Locate every blood parasite and identify its species.
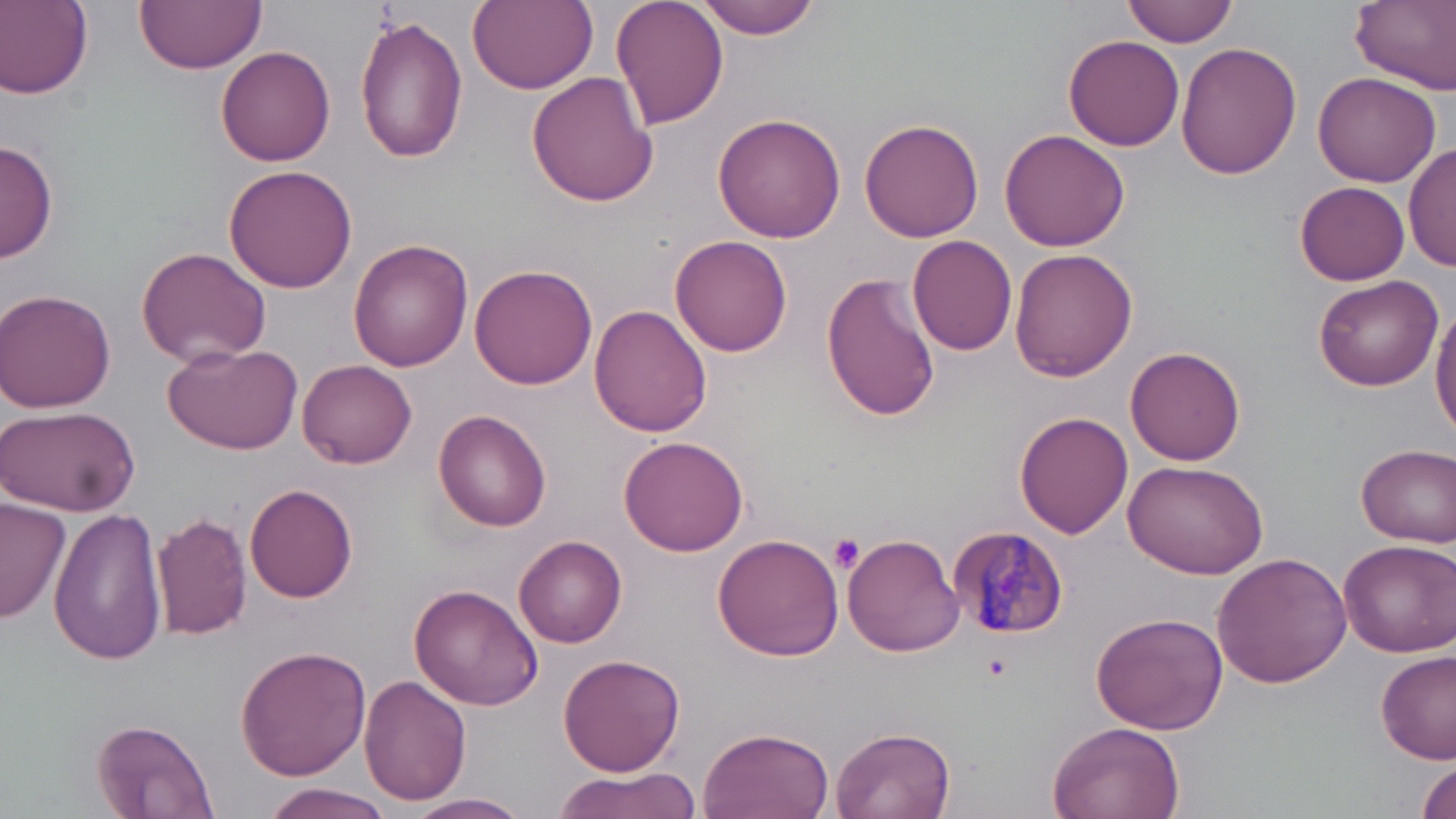

Approximate bounding boxes as (x1, y1, x2, y2) in pixels.
Plasmodium malariae-infected red blood cells: (948, 527, 1069, 640).
No Plasmodium falciparum, Plasmodium ovale, Plasmodium vivax, Babesia divergens, or Trypanosoma brucei observed.

Platelet locations: (829, 534, 865, 571). Uninfected red blood cell locations: (1, 0, 94, 97), (136, 0, 265, 73), (467, 0, 598, 93), (609, 0, 729, 130), (1123, 0, 1238, 46), (1350, 0, 1456, 90), (692, 1, 824, 38), (352, 12, 466, 165), (1063, 34, 1184, 151), (1175, 41, 1304, 180), (217, 46, 337, 167), (1313, 70, 1441, 186), (527, 73, 658, 210), (712, 112, 847, 244), (858, 117, 984, 245), (998, 128, 1131, 253), (0, 140, 57, 264), (1404, 142, 1455, 272), (223, 165, 358, 293), (1295, 181, 1410, 286), (907, 234, 1019, 356), (670, 236, 793, 357), (348, 240, 474, 370), (136, 246, 272, 368), (1010, 248, 1138, 381), (470, 264, 597, 390), (820, 273, 942, 422), (1313, 274, 1443, 391), (2, 290, 118, 412), (590, 304, 712, 438), (1430, 304, 1456, 440), (165, 340, 303, 453), (1126, 347, 1248, 467), (298, 359, 417, 469), (0, 404, 136, 515), (435, 410, 552, 532), (1017, 412, 1133, 540), (619, 432, 750, 557), (1356, 443, 1455, 546), (1120, 458, 1269, 578), (244, 484, 358, 602), (0, 498, 72, 625), (48, 505, 168, 665), (153, 512, 252, 641), (711, 532, 844, 661), (843, 532, 963, 657), (515, 534, 627, 648), (1335, 538, 1454, 658), (1213, 551, 1354, 689), (410, 585, 544, 711), (1090, 609, 1227, 735), (235, 644, 370, 780), (1375, 651, 1454, 765), (558, 653, 685, 774), (360, 676, 471, 807), (91, 716, 218, 818), (1045, 720, 1186, 819), (830, 726, 956, 819), (698, 728, 835, 819), (1413, 760, 1456, 819), (549, 769, 706, 819), (258, 782, 397, 819), (408, 793, 532, 818). Slide-level diagnosis: Plasmodium malariae. Captured at 1000x magnification. May-Grünwald-Giemsa stain. Light microscopy. Single field of view. Thin blood smear. Image is 1456×819 pixels.